Assess the morphology of the red blood cells.
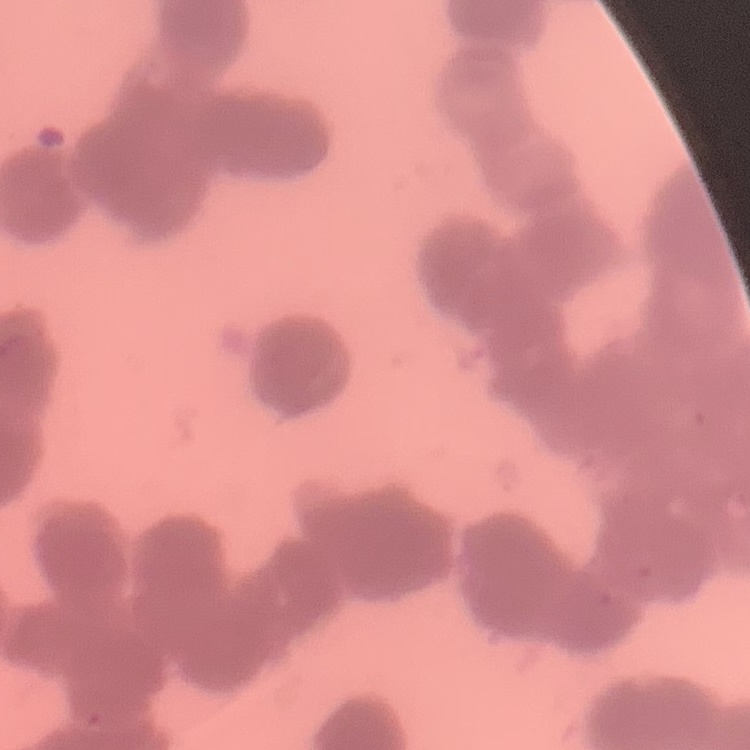
Rouleaux formation.

{
  "image_type": "one tile cut from a larger photomicrograph",
  "preparation": "thin blood film",
  "stain": "Field's or Giemsa"
}